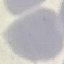 Result: negative for malaria parasites. Acquired by smartphone through the microscope eyepiece. Thin blood film. Giemsa-stained preparation. Automatically extracted cell patch, resized to 64 × 64 pixels.